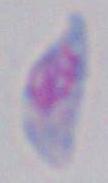

identification = Toxoplasma gondii
magnification = 1000x
modality = photomicrograph